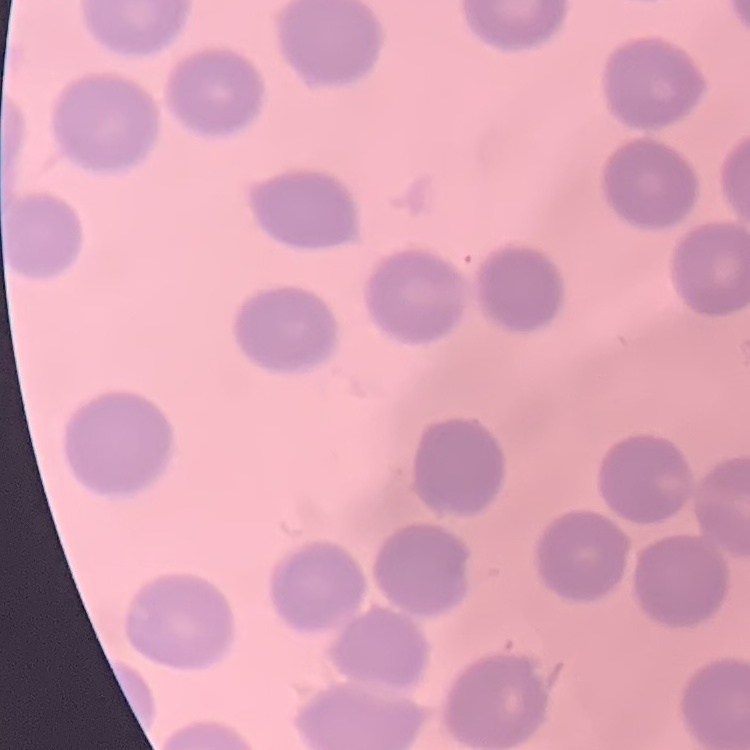 The erythrocytes show no rouleaux formation. One tile cut from a larger photomicrograph. Thin blood film. Stained with either Field's or Giemsa.